Locate every Plasmodium parasite.
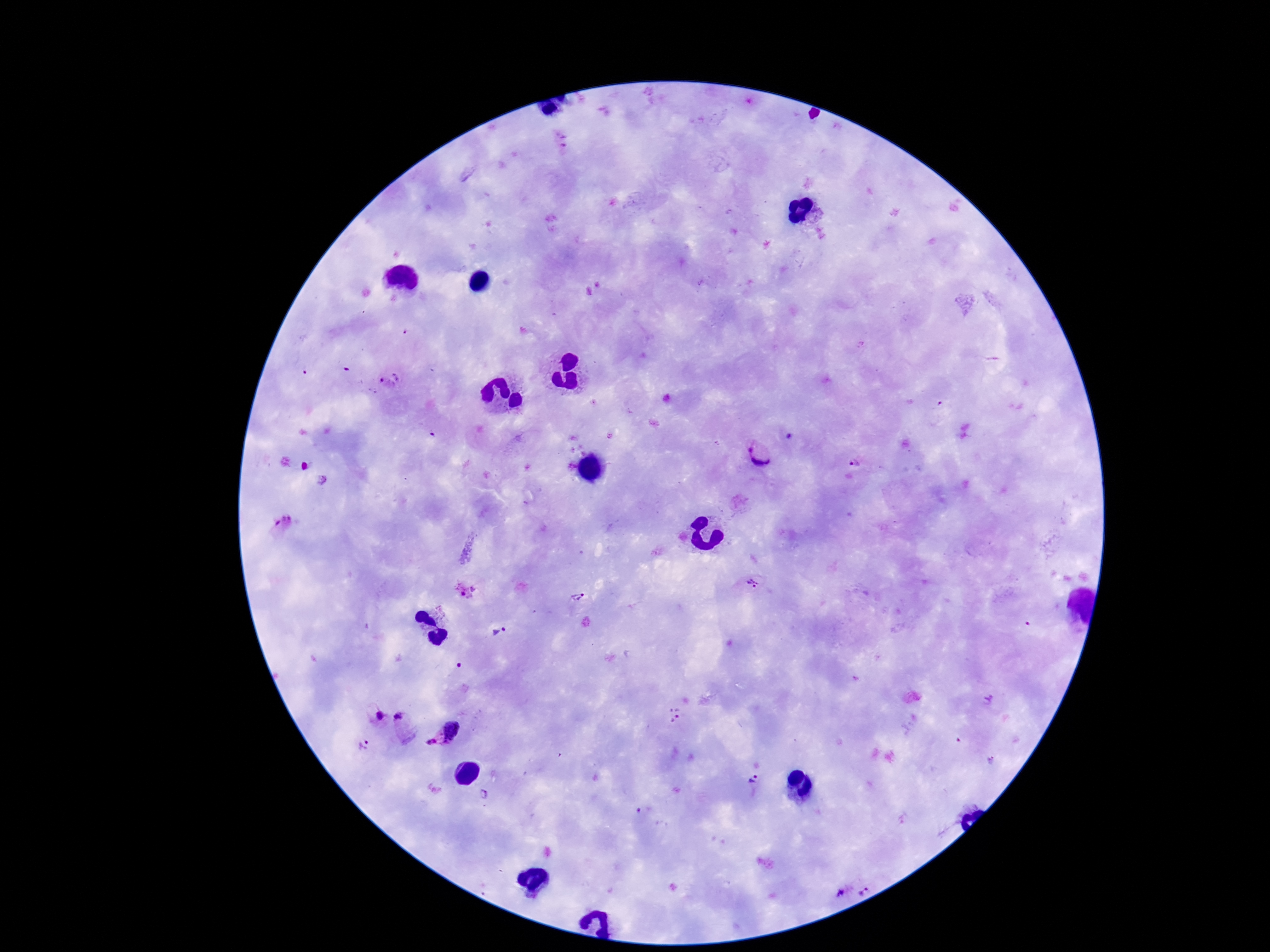

Approximate object centers, in pixels from the top-left corner.
Plasmodium parasites: (x=562, y=139), (x=389, y=381), (x=610, y=435), (x=760, y=453), (x=852, y=463), (x=322, y=479), (x=283, y=521), (x=754, y=581), (x=466, y=589), (x=577, y=597), (x=505, y=628), (x=495, y=633), (x=855, y=679), (x=989, y=700), (x=375, y=712), (x=675, y=713), (x=404, y=724), (x=454, y=730), (x=432, y=743), (x=362, y=745), (x=990, y=759), (x=753, y=780), (x=483, y=794), (x=863, y=891), (x=841, y=892).

patient malaria status = infected
magnification = 100x
preparation = thick blood film
capture = smartphone camera through the microscope eyepiece
field of view = single
stain = Giemsa
image size = 1270×952 pixels